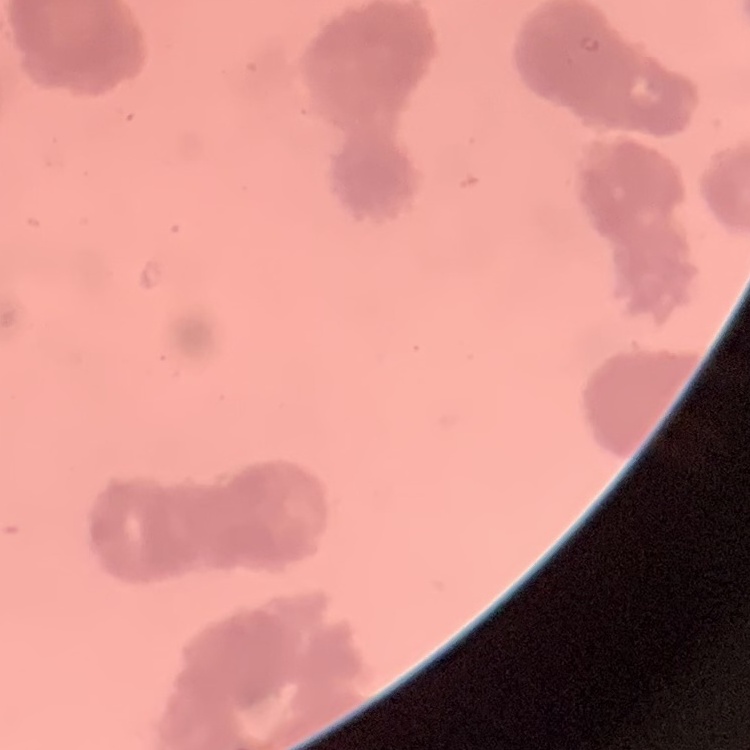
The red blood cells show rouleaux formation. Field's or Giemsa stain. Square crop of a larger photomicrograph. Thin peripheral smear.